Describe the morphology of the red blood cells.
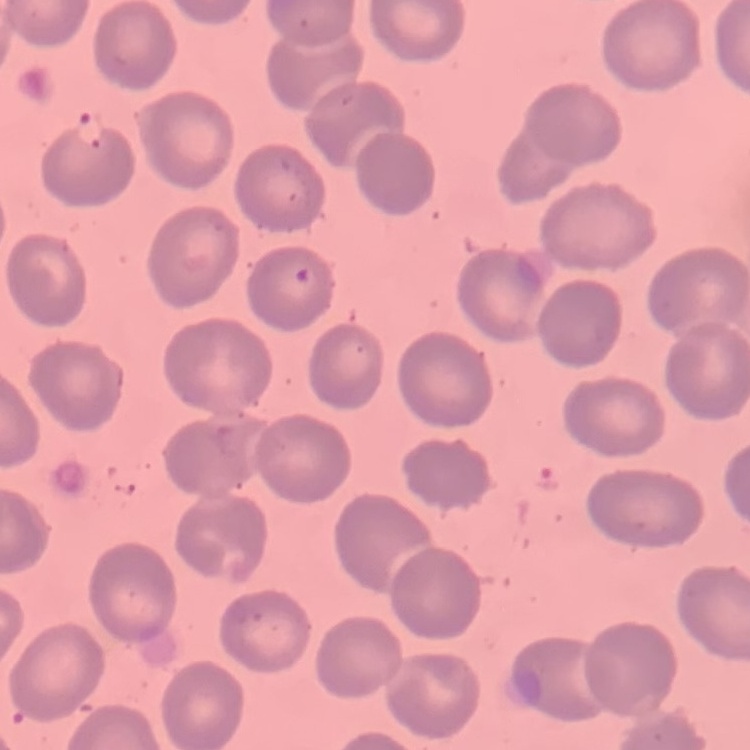

They show no rouleaux formation.

Stained with either Field's or Giemsa. One tile cut from a larger photomicrograph. Thin blood smear.